Assess for parasitized red blood cells.
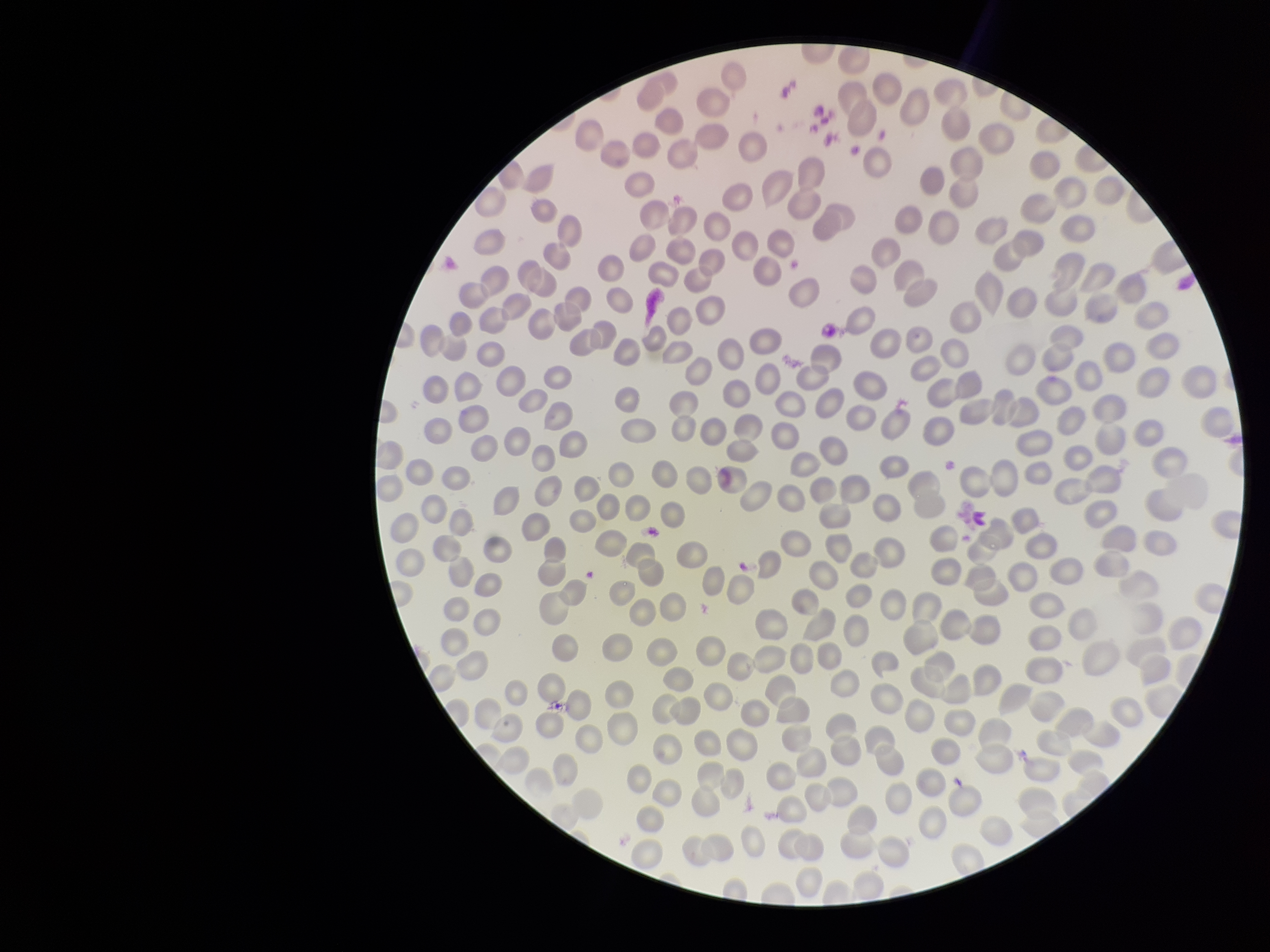

None identified.

Summary:
  - Capture: smartphone photograph through the microscope eyepiece
  - Patient malaria status: negative
  - Parasitized red blood cell count: 0
  - Field of view: single
  - Stain: Giemsa
  - Image size: 1270×952 pixels
  - Red blood cell count: 265
  - Preparation: thin blood smear